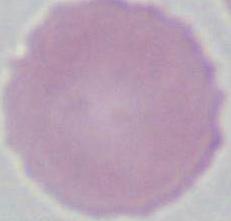
A red blood cell is shown. Captured at 1000x magnification. Micrograph.